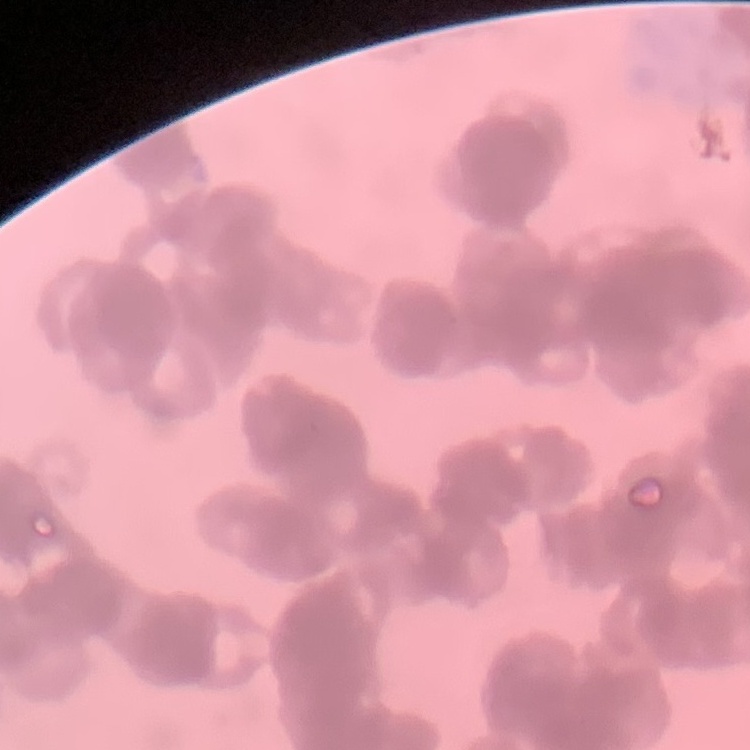
The erythrocytes exhibit rouleaux formation. One tile cut from a larger photomicrograph. Thin blood smear. Stained with either Field's or Giemsa.